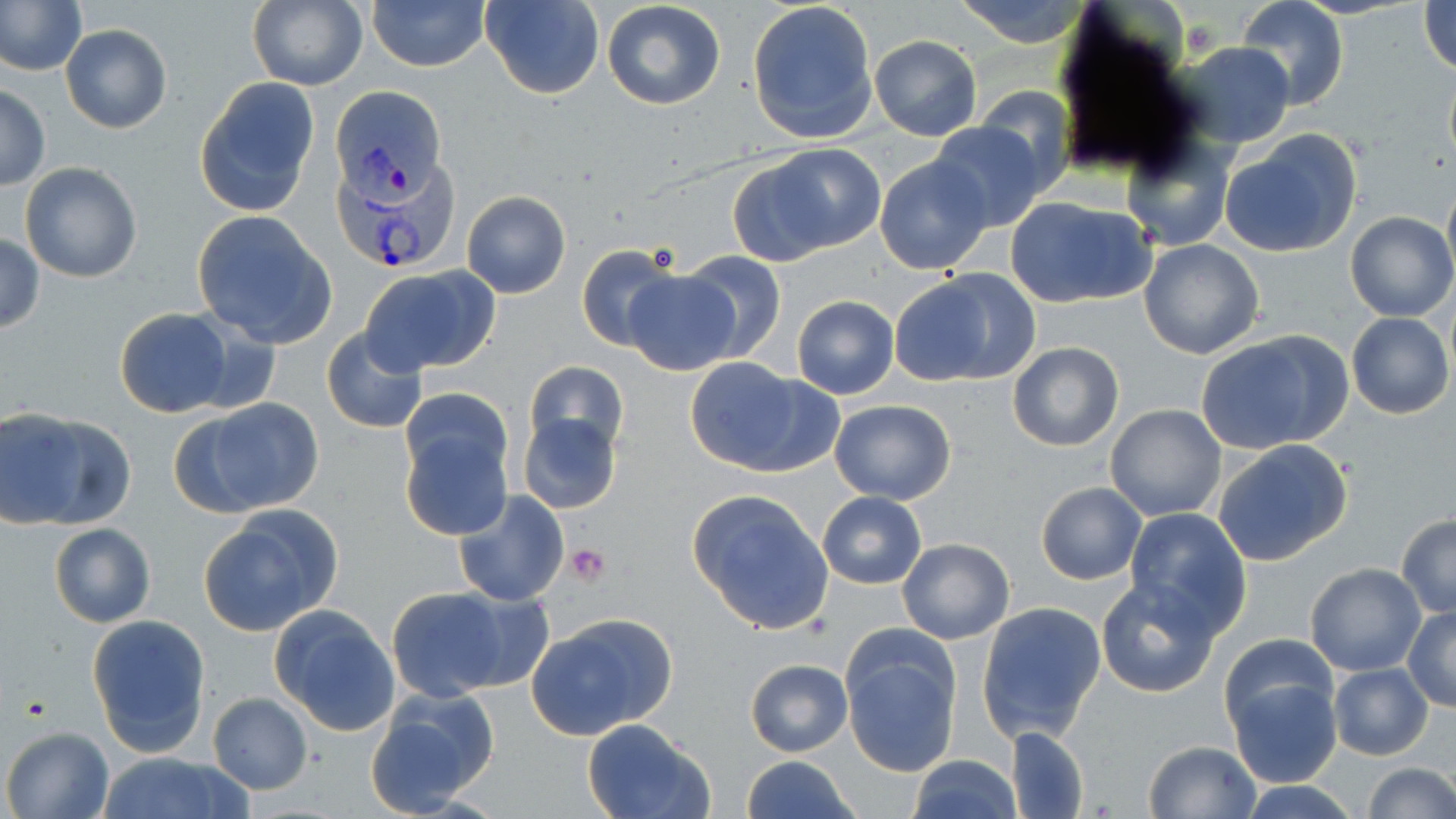

{
  "plasmodium_vivax_infected_red_blood_cell_locations": "approximate bounding boxes as (x1, y1, x2, y2) in pixels: (334, 85, 444, 196), (332, 152, 462, 274)",
  "slide_level_diagnosis": "Plasmodium vivax",
  "magnification": "1000x",
  "image_size": "1456×819 pixels",
  "uninfected_red_blood_cell_locations": "approximate bounding boxes as (x1, y1, x2, y2) in pixels: (482, 0, 602, 100), (746, 0, 878, 143), (953, 0, 1090, 46), (1421, 0, 1455, 77), (0, 1, 85, 76), (246, 1, 368, 90), (369, 1, 489, 72), (601, 1, 726, 111), (1235, 1, 1349, 108), (62, 24, 172, 133), (868, 35, 981, 140), (1168, 41, 1296, 150), (194, 77, 322, 215), (0, 85, 50, 191), (974, 87, 1076, 195), (927, 122, 1047, 232), (1220, 129, 1362, 258), (1122, 139, 1235, 250), (760, 145, 884, 255), (874, 155, 995, 274), (19, 161, 143, 284), (1442, 174, 1456, 287), (461, 191, 571, 299), (1003, 195, 1157, 308), (1346, 210, 1455, 322), (192, 212, 337, 347), (0, 231, 43, 334), (1138, 237, 1265, 360), (577, 245, 680, 353), (679, 250, 786, 363), (359, 264, 499, 378), (890, 269, 1040, 387), (622, 270, 739, 375), (790, 295, 900, 400), (114, 307, 233, 417), (1345, 312, 1454, 419), (321, 327, 428, 434), (1195, 331, 1351, 455), (1008, 343, 1124, 451), (683, 356, 824, 475), (524, 362, 629, 459), (404, 380, 507, 481), (192, 396, 324, 515), (829, 399, 956, 505), (1105, 403, 1227, 521), (0, 410, 101, 527), (517, 412, 622, 515), (399, 417, 513, 541), (1211, 438, 1354, 567), (1036, 481, 1145, 584), (452, 489, 569, 607), (687, 490, 835, 635), (818, 492, 925, 588), (199, 507, 341, 633), (1123, 507, 1251, 636), (1396, 512, 1456, 618), (48, 523, 157, 628), (897, 537, 1015, 644), (1305, 564, 1427, 676), (1095, 577, 1223, 697), (385, 585, 516, 701), (445, 591, 554, 692), (978, 601, 1108, 742), (1403, 604, 1456, 711), (269, 605, 401, 737), (87, 613, 211, 756), (527, 614, 678, 740), (839, 627, 962, 777), (1219, 634, 1340, 741), (744, 657, 853, 758), (1327, 664, 1433, 760), (1224, 675, 1343, 789), (365, 691, 498, 817), (208, 692, 312, 794), (580, 718, 715, 819), (2, 726, 113, 818), (1006, 726, 1088, 818), (1142, 739, 1262, 818), (97, 753, 250, 819), (907, 754, 1020, 819), (741, 755, 860, 819), (1361, 763, 1455, 818), (1236, 781, 1364, 818)",
  "preparation": "thin blood film",
  "modality": "light microscopy",
  "platelet_locations": "approximate bounding boxes as (x1, y1, x2, y2) in pixels: (565, 544, 611, 587)",
  "field_of_view": "single",
  "stain": "May-Grünwald-Giemsa"
}